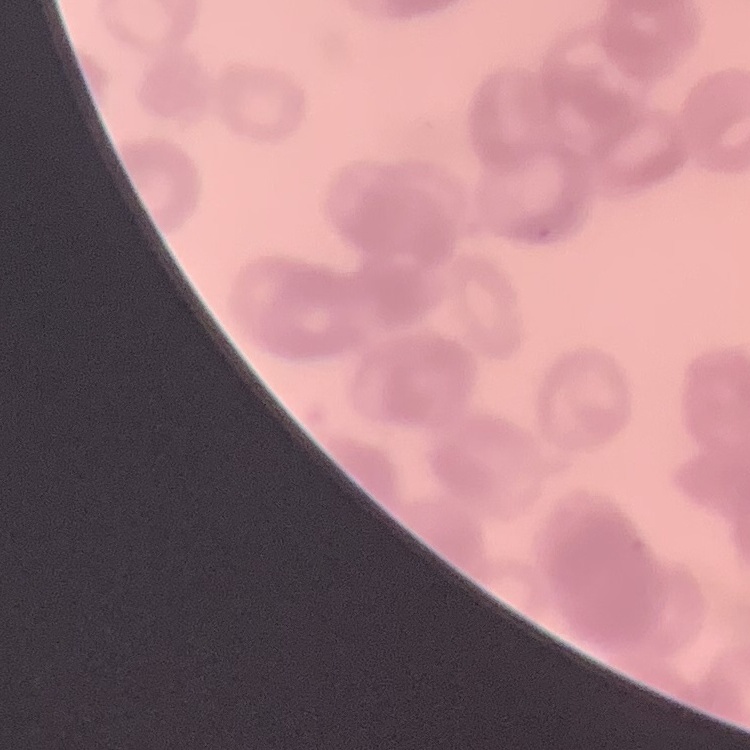

The erythrocytes show rouleaux formation. Square crop of a larger photomicrograph. Stained with either Field's or Giemsa. Thin blood smear.